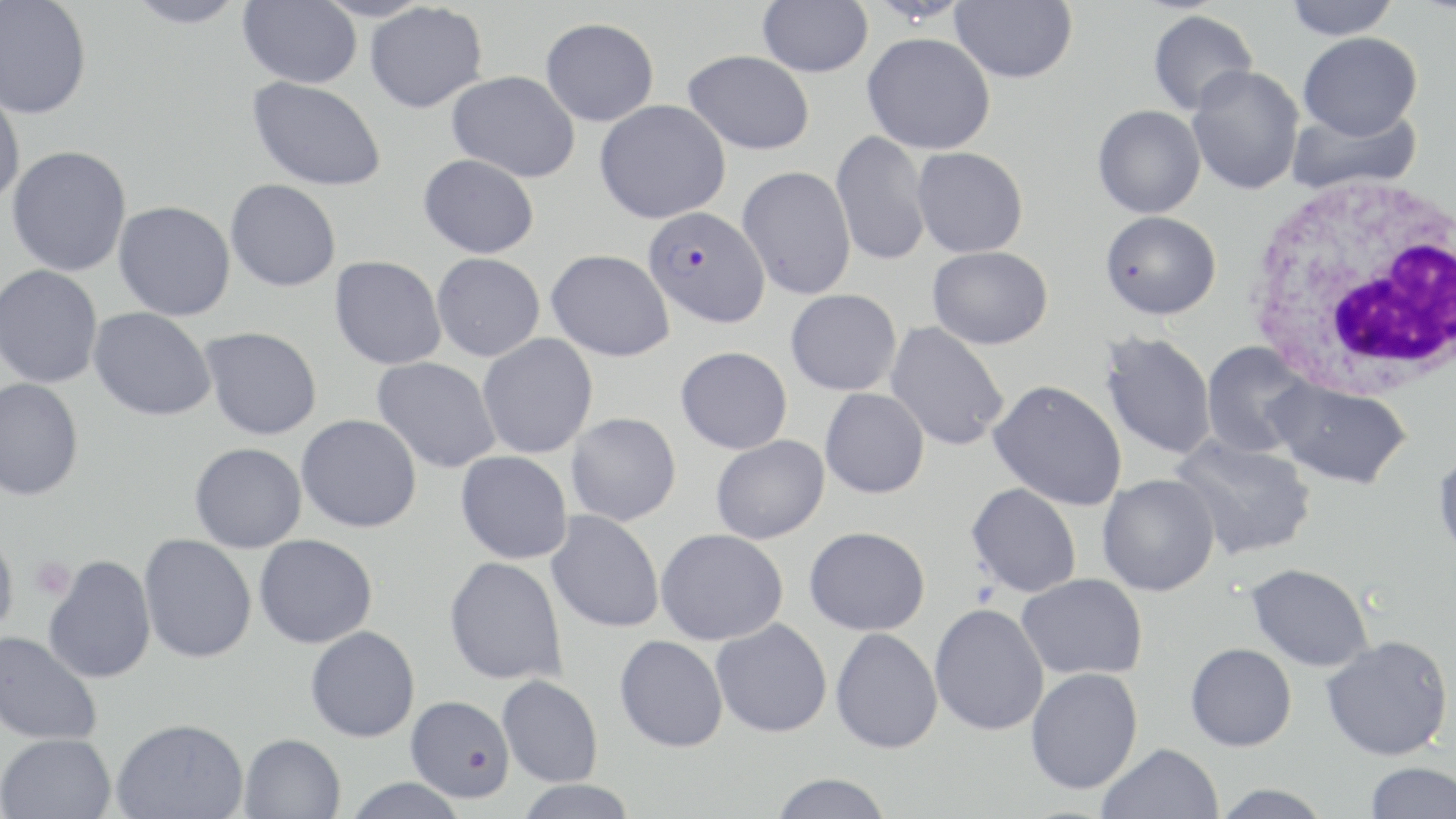
slide-level diagnosis = Plasmodium falciparum
modality = light microscopy
preparation = thin blood film
Plasmodium falciparum-infected red blood cell locations = approximate bounding boxes as (x1,y1)-(x2,y2) corner pairs in pixels: (643,206)-(770,328)
magnification = 1000x
platelet locations = approximate bounding boxes as (x1,y1)-(x2,y2) corner pairs in pixels: (29,556)-(76,601)
stain = May-Grünwald-Giemsa
image size = 1456×819 pixels
uninfected red blood cell locations = approximate bounding boxes as (x1,y1)-(x2,y2) corner pairs in pixels: (0,0)-(93,119), (123,0)-(247,29), (757,0)-(873,77), (1284,0)-(1401,39), (238,1)-(362,88), (949,1)-(1079,84), (365,3)-(488,113), (1147,10)-(1258,116), (541,17)-(659,126), (862,32)-(995,154), (1297,32)-(1423,139), (684,49)-(815,155), (1186,66)-(1305,195), (447,70)-(581,181), (247,76)-(387,192), (0,82)-(26,208), (594,100)-(731,224), (1092,105)-(1205,218), (1286,105)-(1422,194), (831,130)-(932,267), (6,144)-(132,277), (911,147)-(1029,258), (419,153)-(540,258), (737,165)-(856,300), (225,179)-(341,292), (113,200)-(236,321), (1099,210)-(1222,320), (927,245)-(1053,349), (546,249)-(675,362), (431,253)-(545,361), (330,256)-(447,370), (0,264)-(104,388), (785,289)-(902,395), (88,307)-(216,421), (884,321)-(1010,451), (200,326)-(323,440), (1098,330)-(1218,461), (477,334)-(598,458), (1200,342)-(1316,459), (676,346)-(793,454), (372,356)-(502,474), (1265,376)-(1413,489), (0,377)-(84,501), (988,379)-(1127,511), (820,388)-(930,498), (566,412)-(681,526), (296,414)-(422,532), (711,435)-(830,544), (1170,435)-(1317,561), (189,442)-(307,553), (1432,448)-(1456,564), (456,451)-(573,564), (1097,474)-(1220,596), (966,483)-(1082,598), (546,510)-(665,633), (804,526)-(930,635), (0,527)-(19,639), (656,528)-(789,645), (138,533)-(257,663), (254,534)-(378,648), (43,555)-(157,684), (444,556)-(568,686), (1243,563)-(1376,672), (1016,573)-(1148,680), (929,603)-(1050,737), (711,618)-(833,737), (305,625)-(421,742), (830,627)-(943,753), (0,630)-(103,746), (1320,634)-(1454,762), (614,635)-(728,752), (1185,643)-(1297,751), (1025,667)-(1143,794), (497,674)-(604,787), (405,695)-(515,802), (112,717)-(248,819), (0,732)-(117,819), (239,733)-(346,819), (1097,743)-(1224,819), (1364,761)-(1456,819), (769,773)-(894,819), (343,777)-(469,819), (514,779)-(638,819), (1211,783)-(1333,819)
white blood cell locations = approximate bounding boxes as (x1,y1)-(x2,y2) corner pairs in pixels: (1239,173)-(1456,399)
field of view = one of a larger specimen